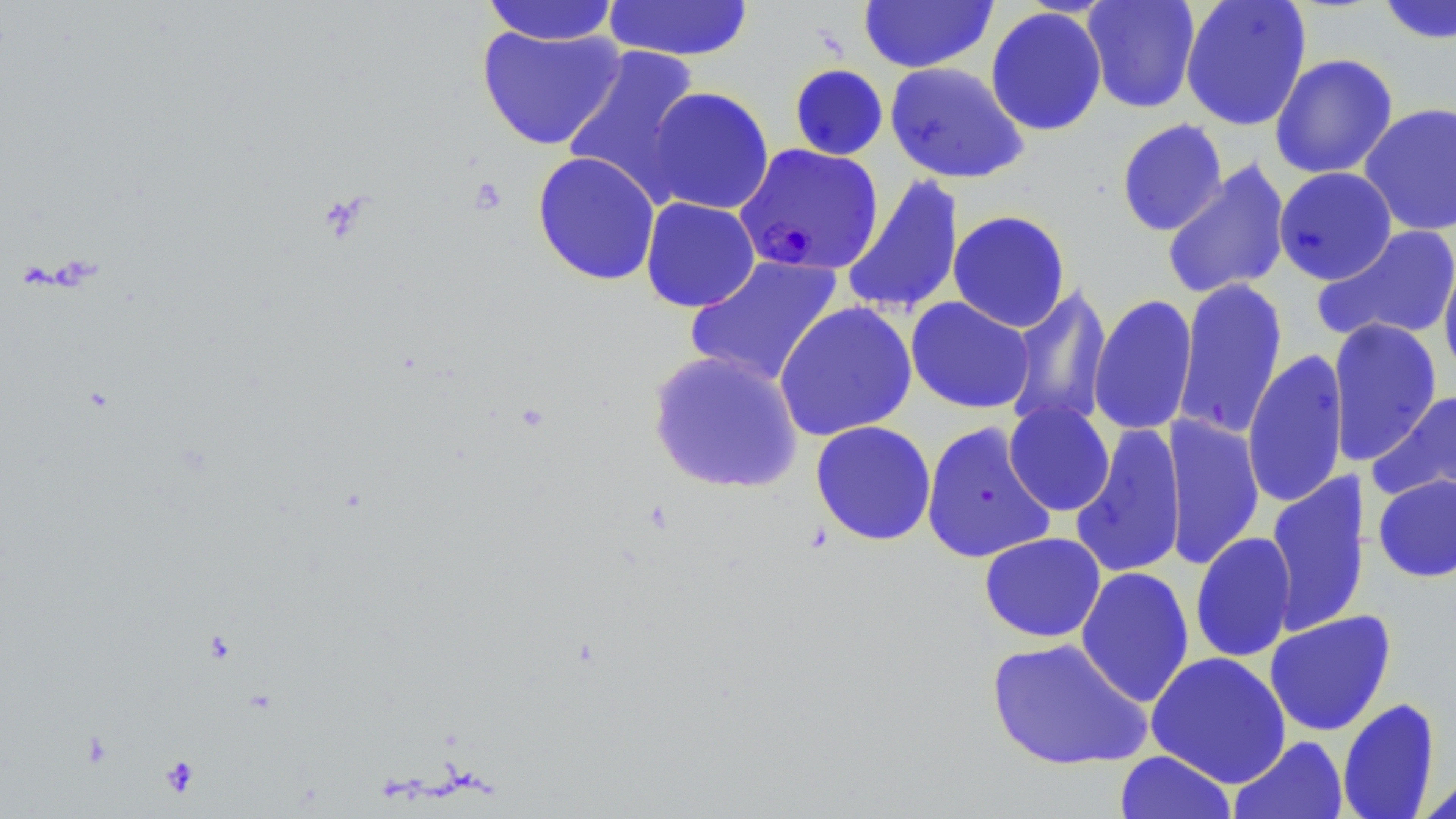

Summary:
  - Coordinate format: approximate bounding boxes as [x1, y1, x2, y2] in pixels
  - Uninfected red blood cell locations: [858, 0, 997, 74], [1082, 0, 1201, 113], [1180, 0, 1312, 131], [482, 1, 621, 45], [602, 1, 755, 62], [1376, 1, 1456, 45], [985, 6, 1107, 137], [476, 24, 626, 151], [562, 45, 703, 202], [1269, 53, 1398, 179], [885, 61, 1028, 184], [788, 63, 889, 161], [644, 87, 775, 215], [1358, 102, 1456, 236], [1116, 119, 1227, 237], [532, 151, 661, 286], [1161, 159, 1292, 300], [1273, 167, 1397, 285], [841, 173, 964, 318], [640, 197, 760, 313], [947, 210, 1071, 332], [1312, 224, 1456, 346], [684, 255, 844, 388], [1438, 255, 1456, 382], [1172, 277, 1288, 440], [1003, 282, 1113, 433], [1088, 294, 1198, 437], [905, 297, 1035, 414], [774, 301, 917, 441], [1328, 318, 1442, 465], [1242, 348, 1349, 510], [647, 350, 803, 494], [1369, 389, 1456, 506], [1003, 401, 1115, 517], [1161, 413, 1264, 570], [810, 420, 937, 547], [920, 421, 1057, 565], [1071, 422, 1186, 579], [1265, 471, 1372, 636], [1373, 474, 1456, 583], [1190, 531, 1297, 664], [979, 532, 1106, 643], [1075, 566, 1195, 708], [1264, 611, 1396, 736], [985, 637, 1154, 771], [1146, 652, 1291, 788], [1336, 698, 1441, 819], [1229, 735, 1349, 819], [1114, 750, 1237, 819], [1419, 771, 1456, 818]
  - Plasmodium falciparum-infected red blood cell locations: [734, 143, 884, 276]
  - Platelet locations: [161, 756, 200, 796]
  - Slide-level diagnosis: Plasmodium falciparum
  - Image size: 1456×819 pixels
  - Stain: May-Grünwald-Giemsa
  - Preparation: thin blood smear
  - Modality: optical microscopy
  - Field of view: single
  - Magnification: 1000x